Report the malaria status of this cell.
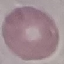
Uninfected.

Thin blood smear. Giemsa-stained preparation. Automatically extracted cell patch, resized to 64 × 64 pixels. Photographed with a smartphone camera at the microscope eyepiece.